Identify the parasite.
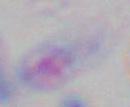
Toxoplasma gondii.

magnification: 1000x
modality: photomicrograph